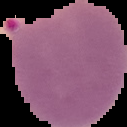
{
  "image_type": "segmented cell region on a black background",
  "preparation": "thin blood smear",
  "image_size": "127×127 pixels",
  "result": "malaria parasites detected"
}